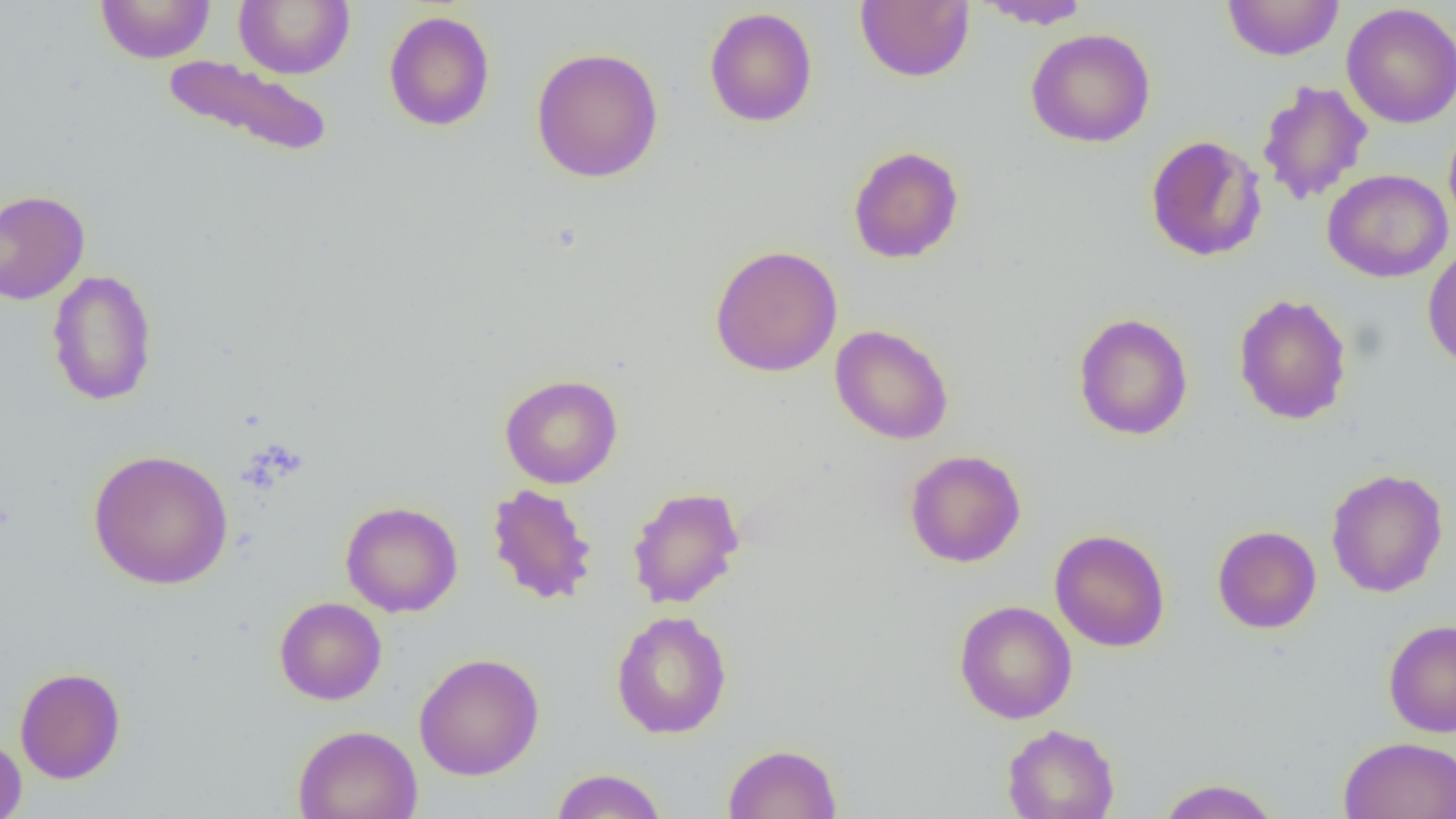

slide-level diagnosis = negative for blood parasites
field of view = one of a larger specimen
preparation = thin blood film
magnification = 1000x
uninfected red blood cell locations = approximate bounding boxes as [x1, y1, x2, y2] in pixels: [95, 0, 216, 64], [234, 0, 355, 79], [855, 0, 974, 83], [978, 0, 1093, 29], [1222, 1, 1344, 61], [1341, 3, 1456, 129], [704, 7, 818, 127], [383, 11, 495, 131], [1025, 28, 1156, 148], [531, 47, 664, 183], [162, 54, 334, 159], [1257, 80, 1373, 206], [1443, 118, 1456, 235], [1145, 135, 1267, 262], [848, 146, 964, 263], [1322, 169, 1453, 283], [0, 189, 90, 305], [709, 244, 843, 377], [1422, 245, 1456, 370], [46, 269, 158, 406], [1233, 293, 1352, 425], [1073, 313, 1193, 440], [830, 324, 954, 445], [499, 374, 623, 489], [87, 448, 234, 590], [904, 449, 1026, 568], [1325, 468, 1449, 598], [486, 483, 598, 605], [627, 485, 745, 609], [340, 501, 463, 617], [1212, 525, 1321, 634], [1049, 529, 1171, 652], [274, 597, 387, 705], [954, 600, 1078, 724], [611, 611, 732, 739], [1383, 619, 1456, 737], [414, 652, 545, 781], [14, 666, 126, 784], [1002, 723, 1120, 819], [293, 724, 422, 819], [0, 734, 27, 819], [1338, 736, 1456, 819], [722, 743, 842, 818], [551, 768, 668, 819], [1154, 778, 1282, 819]
image size = 1456×819 pixels
modality = optical microscopy